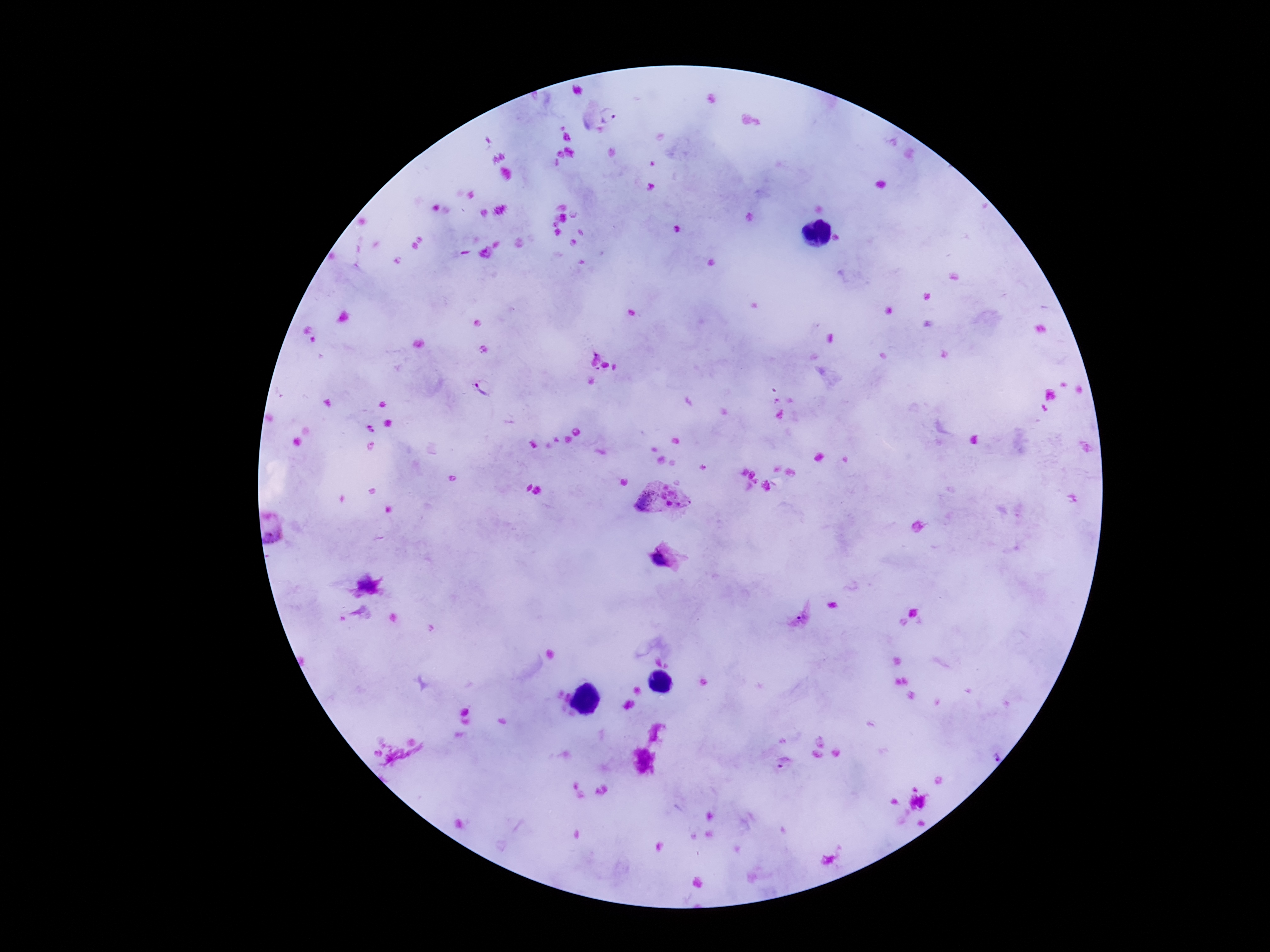

stain = Giemsa
Plasmodium parasite locations = approximate object centers, in pixels from the top-left corner: (x=484, y=389), (x=664, y=502), (x=665, y=559), (x=786, y=763)
preparation = thick blood film
field of view = single
image size = 1270×952 pixels
patient malaria status = infected
magnification = 100x
capture = smartphone camera through the microscope eyepiece